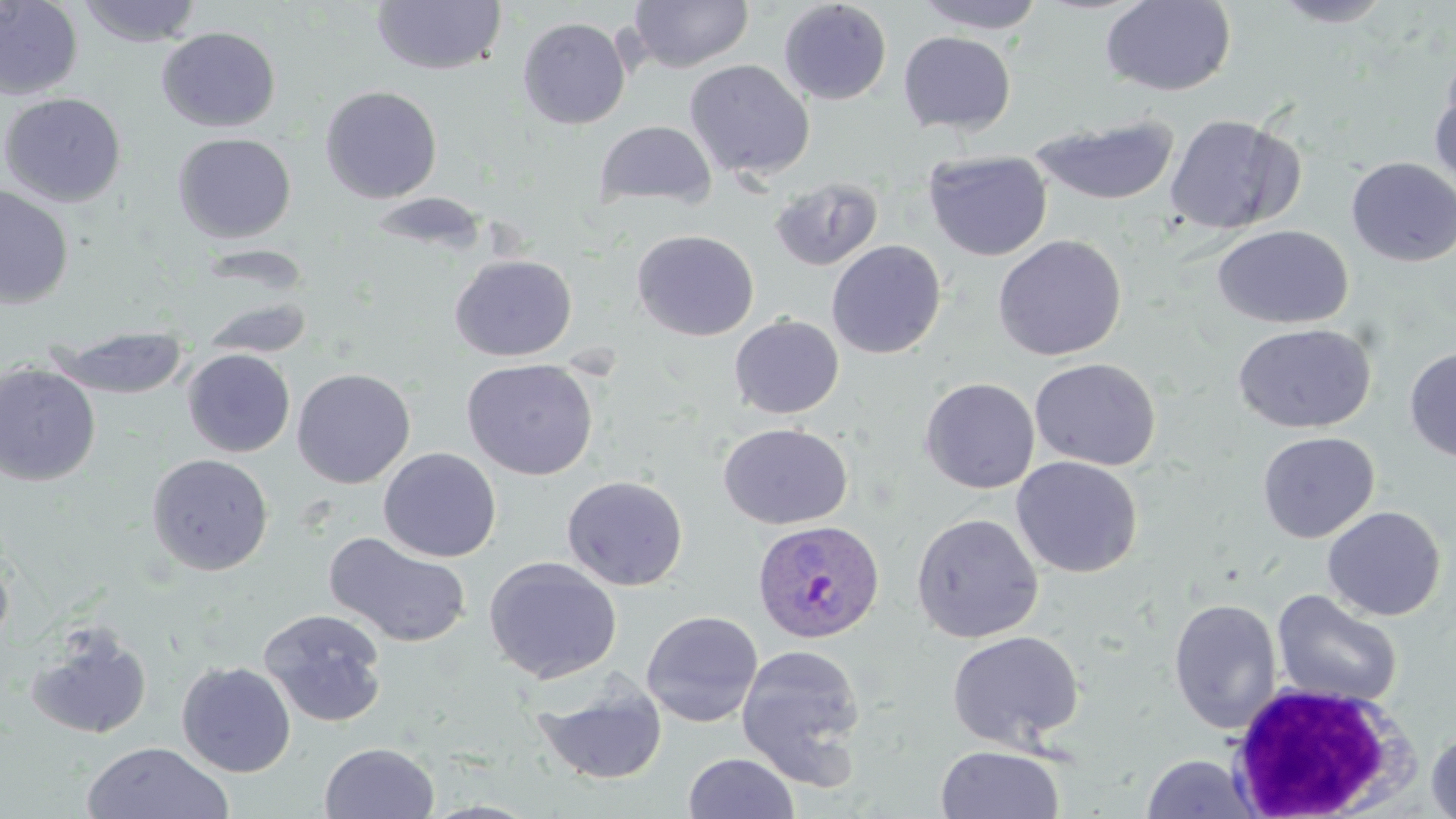 Approximate bounding boxes as (x1,y1)-(x2,y2) corner pairs in pixels. Plasmodium ovale-infected red blood cell locations: (751,518)-(885,644). Uninfected red blood cell locations: (0,0)-(84,100), (75,0)-(204,47), (1100,0)-(1236,96), (1267,0)-(1398,28), (370,1)-(508,76), (628,1)-(753,72), (778,1)-(892,105), (912,1)-(1049,34), (517,17)-(631,130), (156,26)-(281,132), (898,31)-(1016,135), (684,59)-(814,180), (1429,71)-(1456,193), (319,85)-(443,203), (0,92)-(127,207), (1165,113)-(1304,236), (1029,115)-(1181,205), (593,120)-(717,210), (172,132)-(297,243), (924,150)-(1052,261), (1346,156)-(1456,267), (769,177)-(883,272), (0,186)-(75,310), (1212,224)-(1354,329), (631,229)-(759,341), (992,234)-(1127,361), (826,240)-(947,359), (449,253)-(577,361), (200,295)-(313,359), (729,314)-(844,419), (1232,322)-(1376,434), (46,325)-(192,400), (1404,346)-(1456,463), (182,348)-(296,457), (1029,357)-(1161,471), (461,358)-(599,481), (0,362)-(102,486), (292,368)-(416,488), (919,377)-(1040,494), (717,422)-(852,530), (1257,431)-(1379,543), (378,447)-(501,562), (147,453)-(273,575), (1011,456)-(1142,578), (561,474)-(688,591), (1322,506)-(1446,621), (910,512)-(1045,643), (324,531)-(473,648), (0,548)-(15,653), (483,556)-(622,684), (1271,589)-(1403,708), (1168,598)-(1282,734), (258,608)-(389,728), (640,610)-(764,728), (25,624)-(154,741), (947,631)-(1085,749), (735,643)-(868,788), (176,661)-(296,777), (533,677)-(667,786), (1424,725)-(1456,819), (80,741)-(234,819), (320,742)-(440,819), (935,745)-(1065,819), (683,752)-(800,818), (1140,753)-(1262,818). White blood cell locations: (1228,680)-(1418,818). Slide-level diagnosis: Plasmodium ovale. Optical microscopy. 1000x magnification. Single field of view. May-Grünwald-Giemsa-stained preparation. Image is 1456×819 pixels. Thin blood smear.